Outline each Trypanosoma brucei.
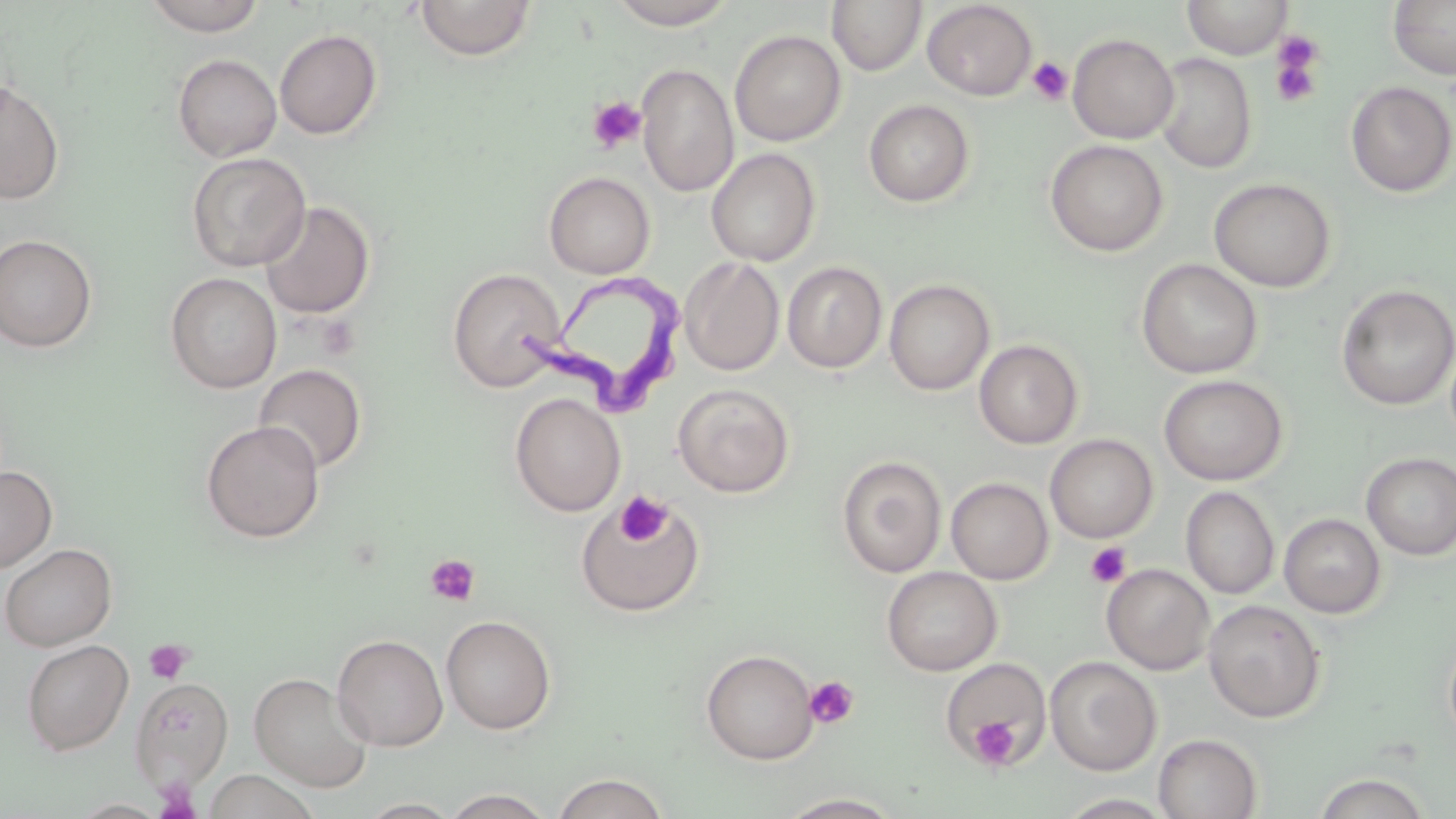

Approximate bounding boxes as [x1, y1, x2, y2] in pixels.
Trypanosoma brucei: [516, 267, 682, 422].

Platelet locations: [1269, 36, 1326, 108], [1027, 57, 1073, 106], [586, 96, 647, 154], [616, 492, 672, 546], [1085, 542, 1131, 588], [425, 554, 481, 607], [144, 639, 191, 684], [804, 676, 859, 729], [970, 715, 1020, 768], [154, 779, 201, 817]. Uninfected red blood cell locations: [143, 0, 267, 36], [607, 0, 738, 29], [1181, 0, 1293, 59], [1387, 0, 1456, 80], [415, 1, 538, 61], [827, 1, 927, 76], [922, 1, 1036, 100], [274, 29, 382, 139], [730, 30, 846, 146], [1068, 33, 1179, 144], [1154, 52, 1257, 173], [173, 54, 282, 162], [636, 63, 739, 197], [0, 81, 65, 204], [1345, 81, 1456, 198], [864, 99, 975, 207], [1045, 139, 1168, 256], [705, 147, 821, 267], [186, 152, 311, 271], [543, 171, 655, 278], [1209, 177, 1336, 292], [259, 200, 375, 319], [0, 234, 97, 352], [680, 256, 784, 376], [1136, 258, 1262, 378], [782, 261, 887, 373], [447, 267, 565, 391], [165, 272, 282, 393], [884, 279, 995, 395], [1336, 283, 1455, 411], [974, 339, 1083, 449], [253, 363, 367, 474], [1159, 374, 1288, 486], [673, 383, 795, 497], [510, 392, 626, 517], [201, 420, 325, 543], [1045, 434, 1158, 543], [1361, 452, 1456, 559], [837, 455, 946, 577], [0, 465, 57, 573], [946, 477, 1053, 584], [1181, 486, 1280, 599], [576, 494, 706, 616], [1279, 513, 1386, 618], [0, 543, 118, 652], [1101, 564, 1215, 675], [881, 566, 1002, 676], [1203, 599, 1326, 722], [440, 614, 557, 735], [1443, 632, 1456, 749], [332, 633, 448, 751], [21, 639, 134, 756], [701, 649, 819, 764], [1045, 656, 1162, 776], [941, 658, 1052, 767], [249, 671, 374, 793], [130, 677, 234, 789], [1153, 733, 1263, 819], [203, 769, 319, 818], [551, 773, 670, 818], [1312, 773, 1432, 818], [441, 788, 556, 818], [778, 792, 904, 818], [1056, 793, 1177, 818], [358, 798, 463, 818]. Slide-level diagnosis: Trypanosoma brucei. 1000x magnification. Image is 1456×819 pixels. May-Grünwald-Giemsa stain. Thin blood smear. Optical microscopy. Single field of view.